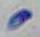
identification = Toxoplasma gondii
modality = micrograph
magnification = 1000x